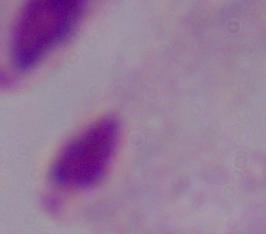

Summary:
  - Magnification: 1000x
  - Identification: trichomonad
  - Modality: photomicrograph